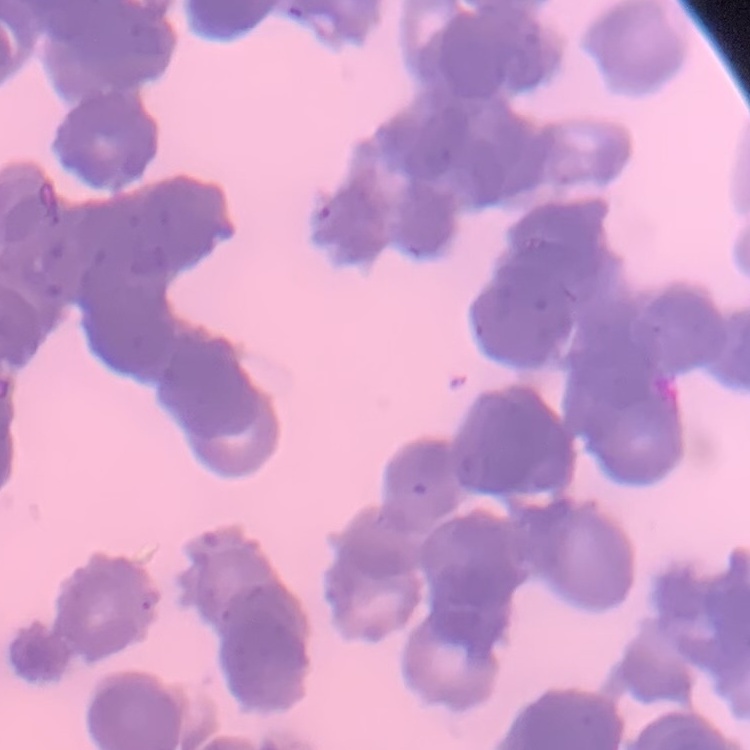
Summary:
  - Red blood cell morphology: rouleaux formation
  - Preparation: thin blood smear
  - Image type: square crop of a larger photomicrograph
  - Stain: Field's or Giemsa